Comment on the morphology of the erythrocytes.
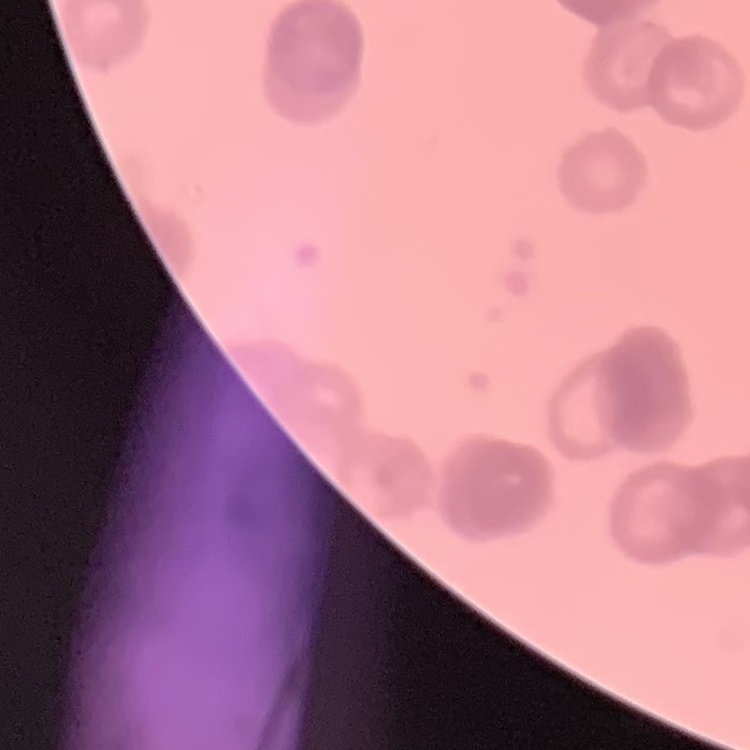
Rouleaux formation.

image type = square crop of a larger photomicrograph
preparation = thin blood smear
stain = Field's or Giemsa